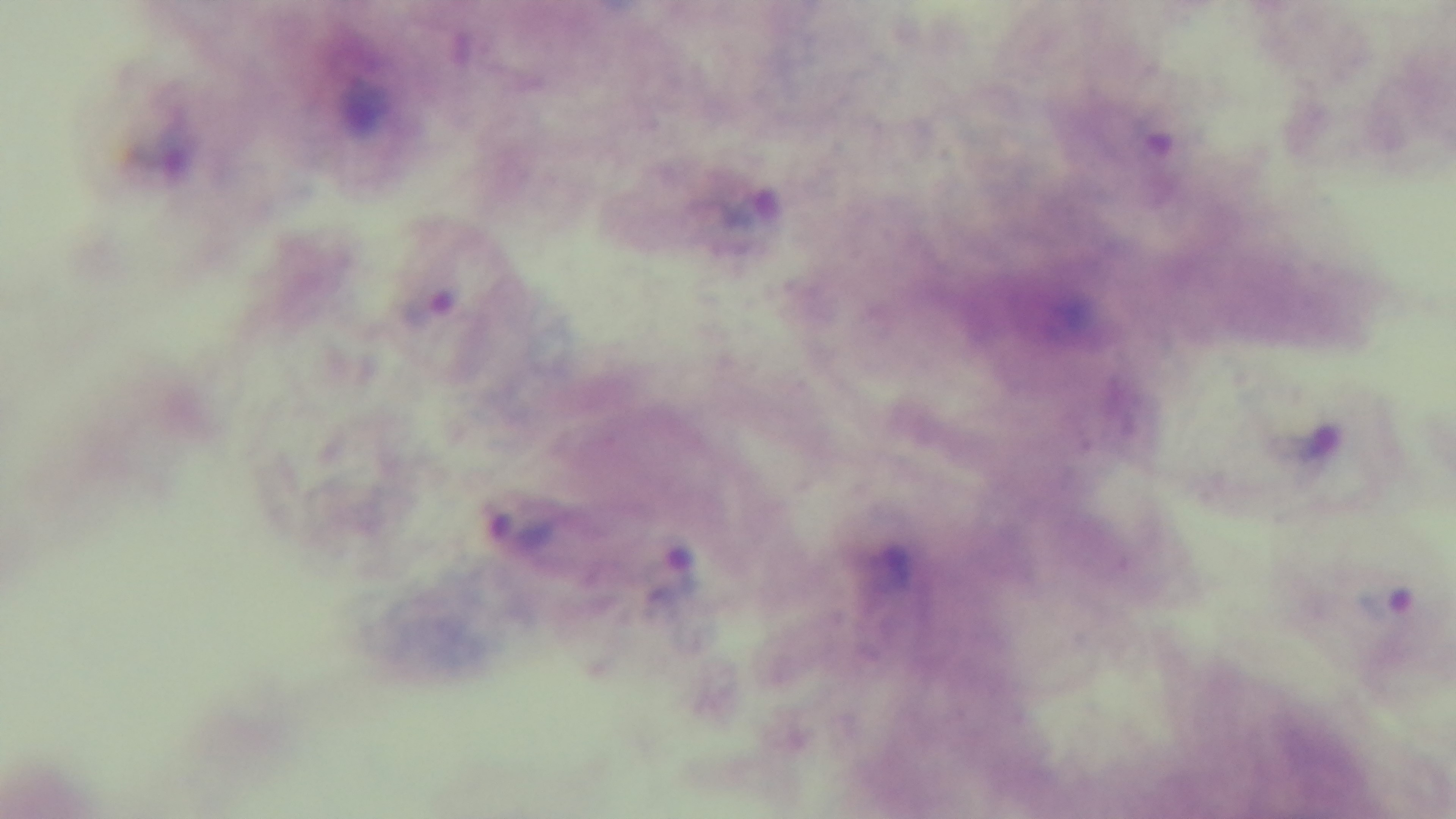

Summary:
  - Preparation: thick
  - Modality: light microscopy
  - Capture: mounted 4K digital camera
  - Objective: 100x oil immersion
  - Malaria status: infected
  - Field of view: one from the slide
  - Stain: Giemsa